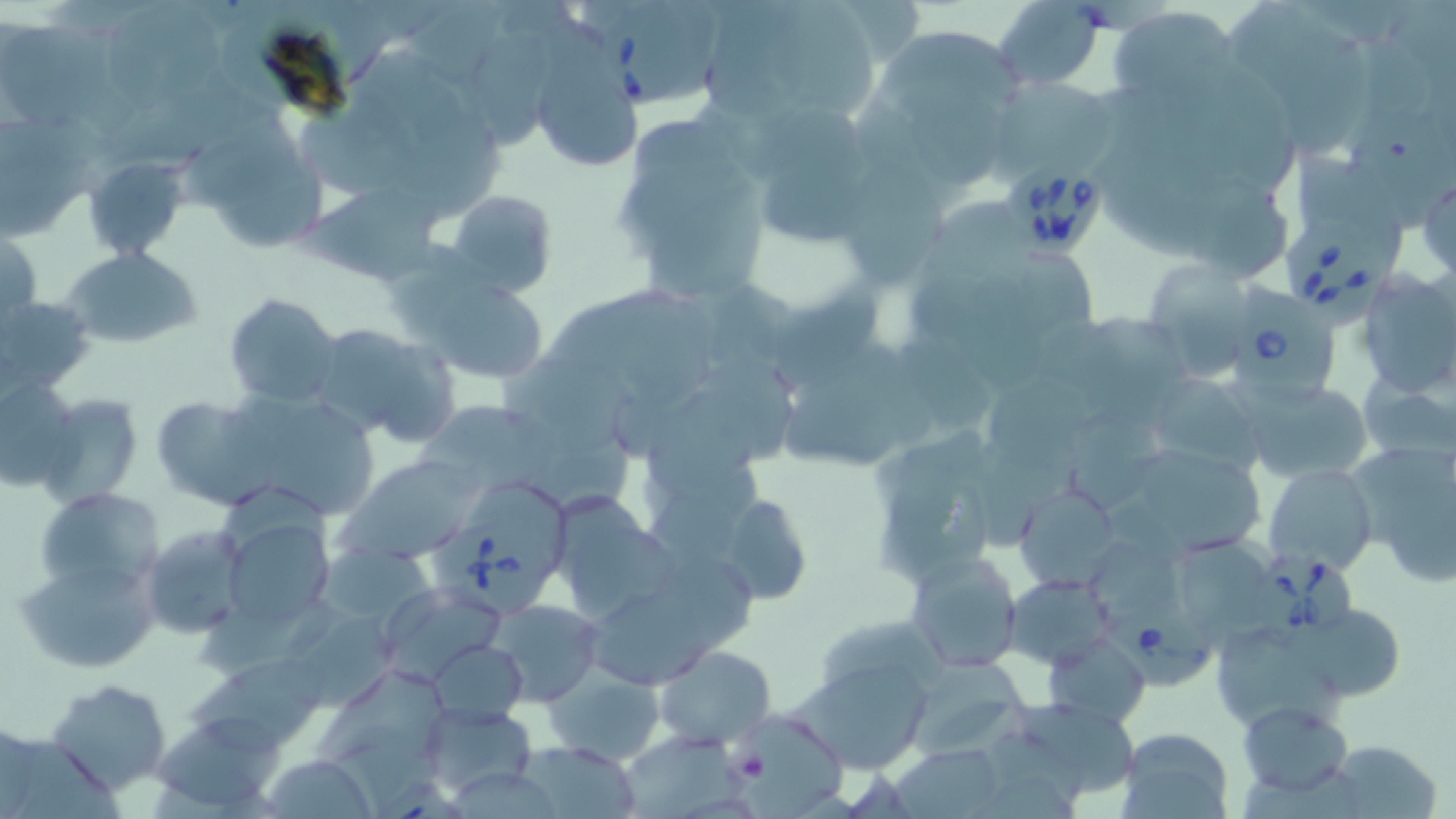

slide_level_diagnosis: Babesia divergens
platelet_locations: 'approximate bounding boxes as named x1/y1/x2/y2 corners in pixels: (x1=728, y1=745, x2=770, y2=786)'
uninfected_red_blood_cell_locations: 'approximate bounding boxes as named x1/y1/x2/y2 corners in pixels: (x1=409, y1=0, x2=509, y2=86), (x1=704, y1=0, x2=799, y2=123), (x1=776, y1=0, x2=880, y2=121), (x1=1236, y1=0, x2=1371, y2=157), (x1=991, y1=1, x2=1108, y2=92), (x1=110, y1=5, x2=225, y2=110), (x1=1106, y1=7, x2=1244, y2=114), (x1=883, y1=23, x2=1023, y2=111), (x1=2, y1=25, x2=137, y2=134), (x1=542, y1=25, x2=636, y2=165), (x1=464, y1=32, x2=552, y2=147), (x1=988, y1=74, x2=1117, y2=181), (x1=908, y1=91, x2=1011, y2=190), (x1=301, y1=103, x2=427, y2=198), (x1=1342, y1=109, x2=1456, y2=224), (x1=388, y1=112, x2=496, y2=215), (x1=633, y1=119, x2=724, y2=178), (x1=3, y1=120, x2=115, y2=230), (x1=185, y1=133, x2=311, y2=208), (x1=1294, y1=149, x2=1408, y2=267), (x1=757, y1=153, x2=888, y2=244), (x1=88, y1=157, x2=182, y2=253), (x1=229, y1=162, x2=331, y2=256), (x1=851, y1=167, x2=949, y2=288), (x1=1191, y1=179, x2=1288, y2=273), (x1=307, y1=181, x2=448, y2=289), (x1=447, y1=190, x2=558, y2=301), (x1=647, y1=214, x2=769, y2=300), (x1=0, y1=230, x2=42, y2=335), (x1=62, y1=247, x2=203, y2=349), (x1=1152, y1=263, x2=1246, y2=373), (x1=1355, y1=270, x2=1455, y2=399), (x1=421, y1=277, x2=551, y2=383), (x1=773, y1=289, x2=881, y2=390), (x1=223, y1=292, x2=341, y2=407), (x1=1, y1=294, x2=96, y2=396), (x1=612, y1=296, x2=715, y2=411), (x1=1084, y1=316, x2=1197, y2=417), (x1=304, y1=323, x2=455, y2=446), (x1=906, y1=337, x2=994, y2=431), (x1=499, y1=360, x2=636, y2=454), (x1=1358, y1=369, x2=1456, y2=465), (x1=983, y1=370, x2=1097, y2=474), (x1=1143, y1=373, x2=1267, y2=474), (x1=0, y1=374, x2=82, y2=491), (x1=1238, y1=379, x2=1373, y2=486), (x1=785, y1=386, x2=910, y2=467), (x1=248, y1=393, x2=377, y2=514), (x1=36, y1=394, x2=142, y2=507), (x1=148, y1=395, x2=263, y2=509), (x1=422, y1=401, x2=560, y2=490), (x1=646, y1=407, x2=767, y2=500), (x1=1065, y1=409, x2=1164, y2=506), (x1=340, y1=455, x2=482, y2=562), (x1=1142, y1=455, x2=1264, y2=555), (x1=1262, y1=464, x2=1378, y2=576), (x1=1388, y1=471, x2=1456, y2=588), (x1=1015, y1=483, x2=1121, y2=592), (x1=876, y1=485, x2=990, y2=576), (x1=33, y1=486, x2=162, y2=598), (x1=548, y1=490, x2=674, y2=620), (x1=716, y1=490, x2=817, y2=609), (x1=224, y1=518, x2=334, y2=631), (x1=141, y1=524, x2=250, y2=638), (x1=1178, y1=536, x2=1275, y2=632), (x1=1090, y1=541, x2=1191, y2=632), (x1=314, y1=547, x2=441, y2=648), (x1=907, y1=552, x2=1025, y2=673), (x1=17, y1=557, x2=158, y2=673), (x1=666, y1=558, x2=753, y2=650), (x1=1005, y1=573, x2=1119, y2=667), (x1=378, y1=584, x2=510, y2=684), (x1=199, y1=595, x2=345, y2=676), (x1=487, y1=599, x2=603, y2=706), (x1=1295, y1=600, x2=1402, y2=700), (x1=591, y1=602, x2=718, y2=684), (x1=282, y1=609, x2=398, y2=709), (x1=821, y1=623, x2=948, y2=687), (x1=1222, y1=627, x2=1347, y2=733), (x1=1046, y1=633, x2=1148, y2=725), (x1=431, y1=640, x2=526, y2=721), (x1=653, y1=645, x2=775, y2=749), (x1=909, y1=654, x2=1038, y2=758), (x1=795, y1=658, x2=936, y2=775), (x1=192, y1=660, x2=337, y2=750), (x1=544, y1=666, x2=664, y2=765), (x1=320, y1=672, x2=449, y2=765), (x1=45, y1=678, x2=174, y2=799), (x1=1005, y1=696, x2=1141, y2=802), (x1=1239, y1=699, x2=1353, y2=799), (x1=421, y1=702, x2=537, y2=799), (x1=724, y1=708, x2=849, y2=815), (x1=152, y1=719, x2=282, y2=808), (x1=1116, y1=727, x2=1235, y2=819), (x1=624, y1=733, x2=751, y2=818), (x1=1324, y1=738, x2=1443, y2=818), (x1=15, y1=739, x2=118, y2=819), (x1=515, y1=741, x2=643, y2=816), (x1=894, y1=744, x2=1008, y2=819), (x1=261, y1=757, x2=379, y2=817), (x1=450, y1=769, x2=558, y2=819)'
preparation: thin blood smear
modality: light microscopy
babesia_divergens_infected_red_blood_cell_locations: 'approximate bounding boxes as named x1/y1/x2/y2 corners in pixels: (x1=593, y1=5, x2=707, y2=107), (x1=997, y1=164, x2=1109, y2=262), (x1=1283, y1=214, x2=1383, y2=332), (x1=1235, y1=276, x2=1332, y2=404), (x1=427, y1=519, x2=551, y2=616), (x1=1245, y1=551, x2=1358, y2=650), (x1=1112, y1=606, x2=1216, y2=689)'
image_size: 1456×819 pixels
field_of_view: one of a larger specimen
stain: May-Grünwald-Giemsa
magnification: 1000x